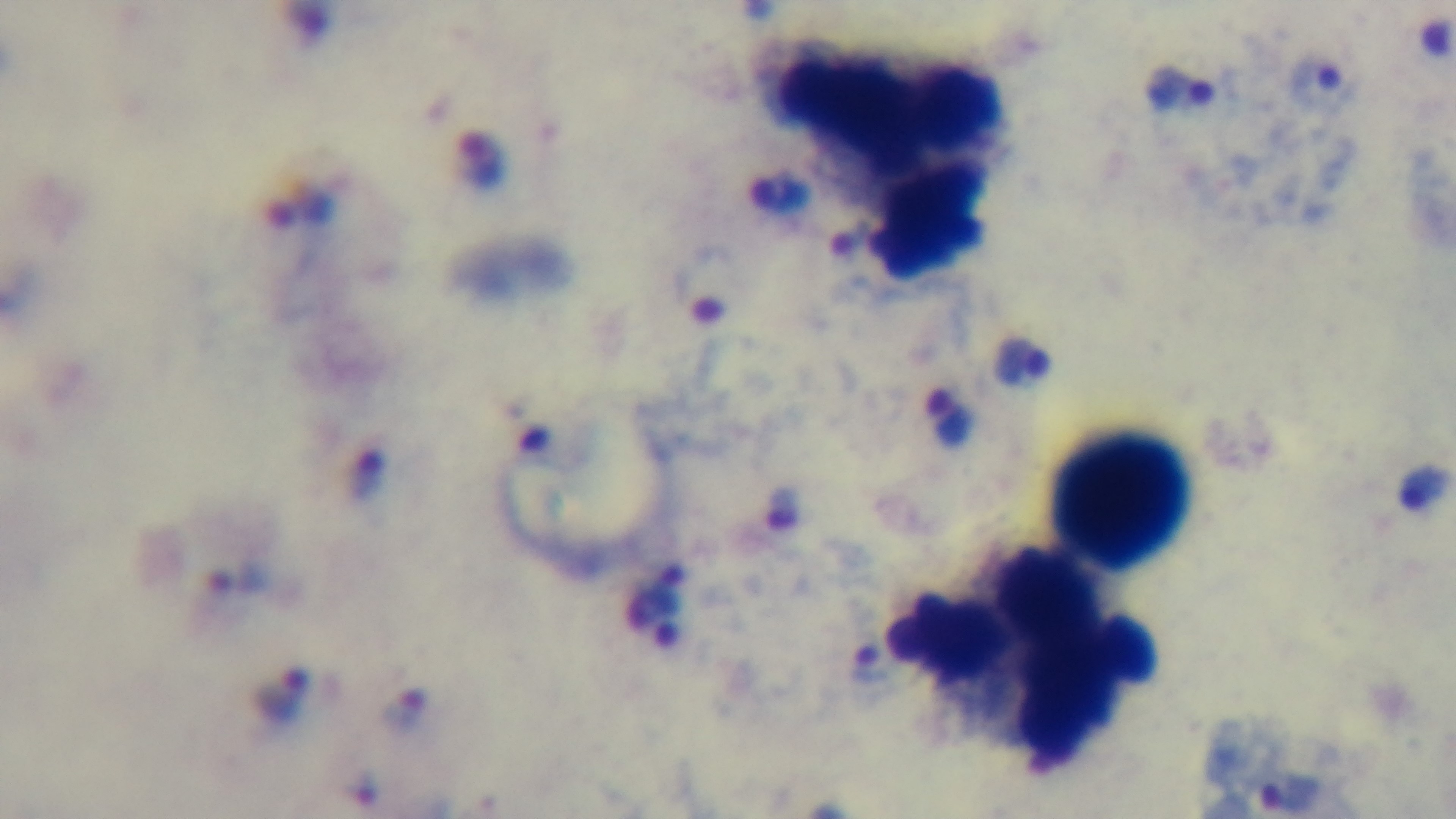
Summary:
  - Field of view: single
  - Malaria status: positive
  - Stain: Giemsa
  - Objective: 100x oil immersion
  - Preparation: thick
  - Capture: mounted 4K digital camera
  - Modality: light microscopy